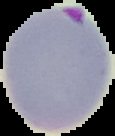

{
  "image_size": "115×136 pixels",
  "result": "Plasmodium parasites identified",
  "preparation": "thin blood film",
  "image_type": "segmented cell region on a black background"
}